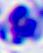
A white blood cell is shown. Photomicrograph. 400x magnification.